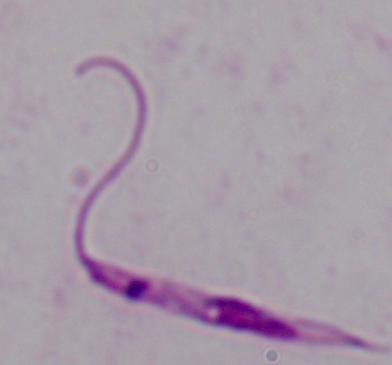
Summary:
  - Modality: micrograph
  - Magnification: 1000x
  - Identification: Leishmania